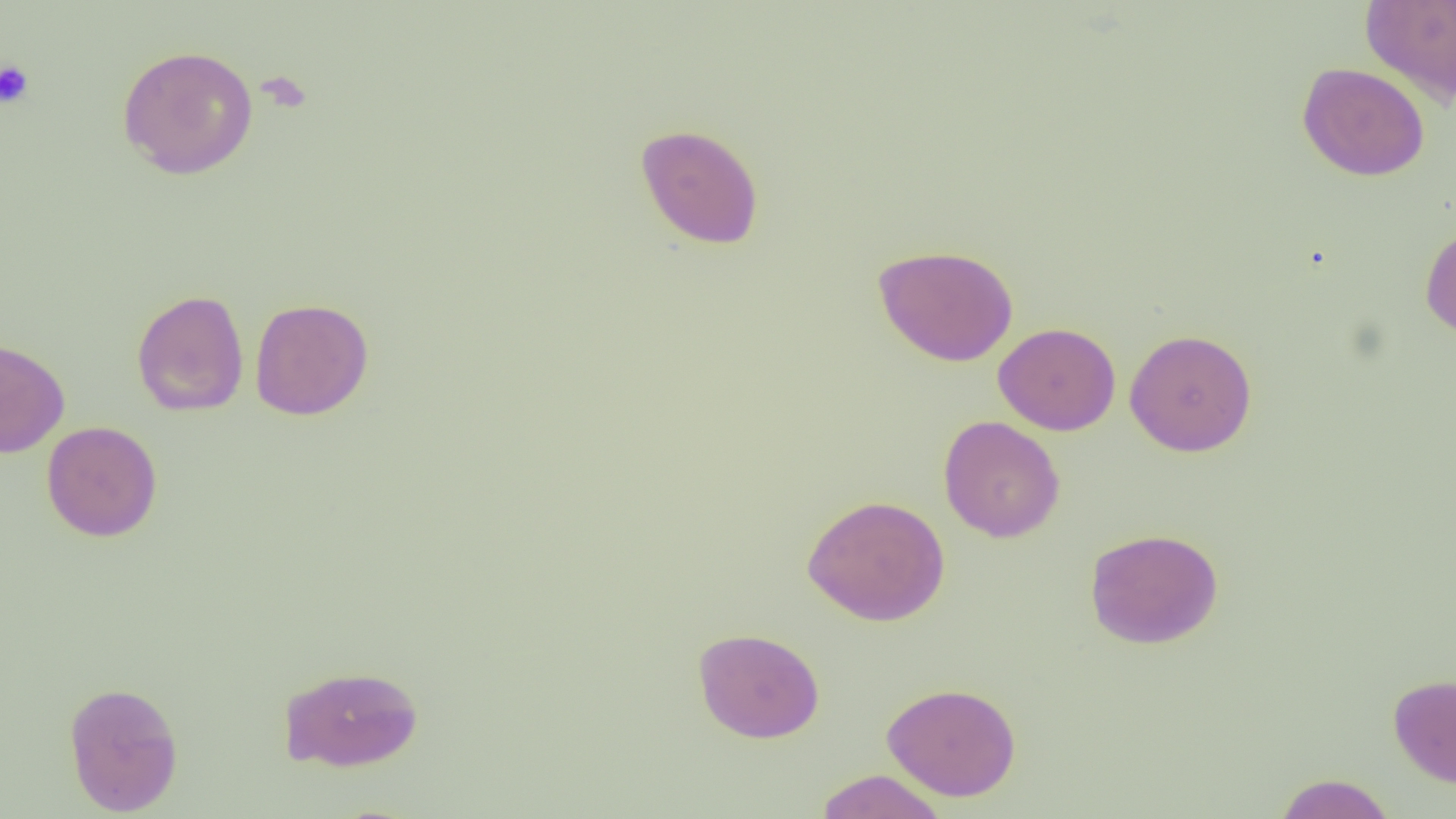 Approximate bounding boxes as (x1, y1, x2, y2) in pixels. Platelet locations: (0, 60, 35, 109). Uninfected red blood cell locations: (1360, 0, 1456, 107), (117, 44, 258, 180), (1297, 62, 1430, 181), (635, 123, 764, 250), (1419, 224, 1456, 341), (873, 244, 1019, 366), (131, 289, 249, 417), (249, 298, 374, 420), (993, 322, 1121, 435), (1124, 328, 1257, 456), (0, 336, 70, 458), (938, 415, 1066, 543), (41, 421, 162, 542), (802, 494, 950, 626), (1085, 528, 1223, 649), (693, 627, 825, 743), (279, 664, 424, 772), (1388, 673, 1456, 788), (63, 680, 184, 816), (881, 682, 1021, 801), (814, 769, 948, 819), (1273, 773, 1396, 819). Slide-level diagnosis: no evidence of blood parasites. Thin blood smear. One field of a larger specimen. 1000x magnification. Light microscopy. Image is 1456×819 pixels.